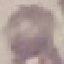

result: no malaria parasites seen
preparation: thin smear
image_type: cell patch, automatically extracted from a larger field of view and resized to 64 × 64 pixels
capture: smartphone through the microscope eyepiece
stain: Giemsa